Assess the morphology of the erythrocytes.
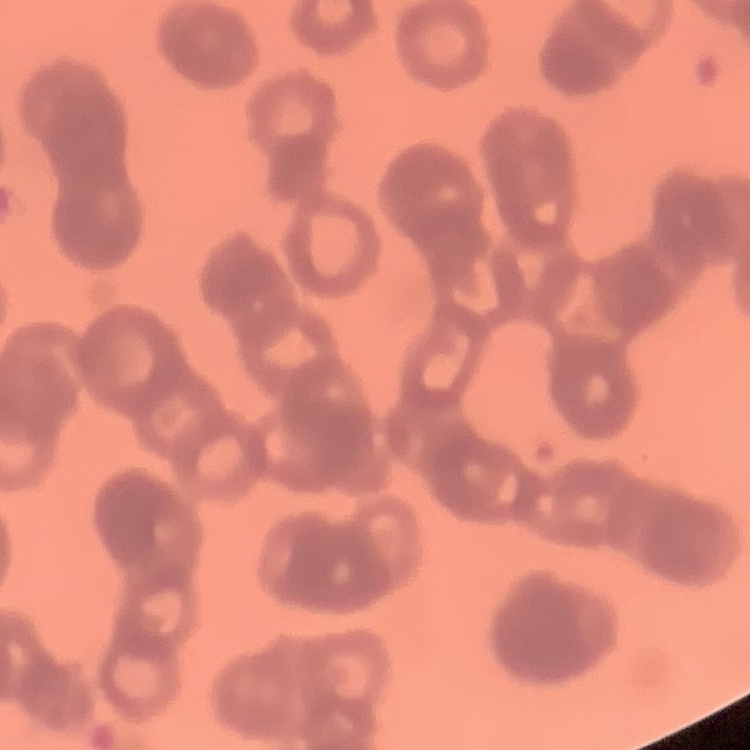
Rouleaux formation.

Summary:
  - Stain: Field's or Giemsa
  - Image type: square crop of a larger photomicrograph
  - Preparation: thin blood film